Identify the cell.
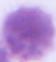

This is an erythrocyte.

modality = micrograph
magnification = 1000x